Identify the cell.
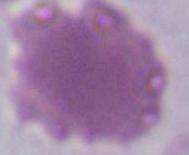

An erythrocyte.

Photomicrograph. Captured at 1000x magnification.